Assess the morphology of the red blood cells.
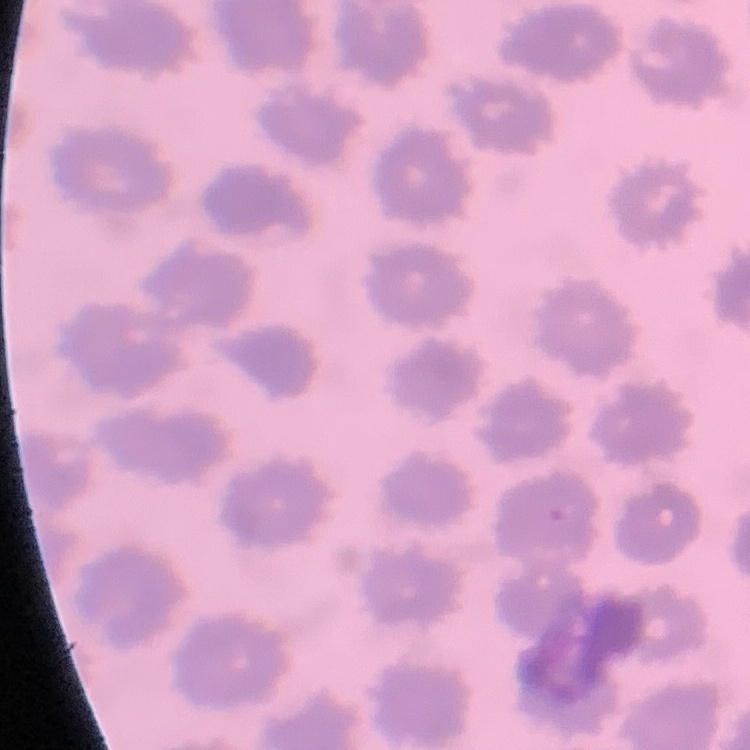

They show no rouleaux formation.

Thin blood film. Stained with either Field's or Giemsa. One tile cut from a larger photomicrograph.